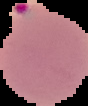

Summary:
  - Preparation: thin blood film
  - Image size: 88×106 pixels
  - Image type: segmented cell region with the area outside set to black
  - Result: malaria parasites detected